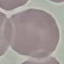 Malaria status: uninfected. Photographed with a smartphone camera at the microscope eyepiece. Thin smear of blood. Automatically extracted cell patch, resized to 64 × 64 pixels. Giemsa-stained preparation.